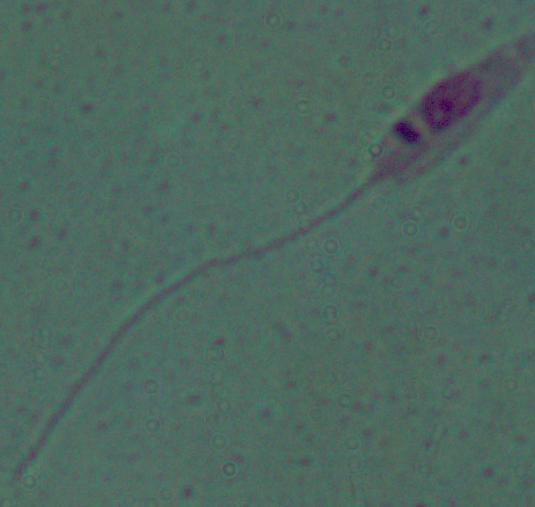

Summary:
  - Modality: micrograph
  - Magnification: 1000x
  - Identification: Leishmania